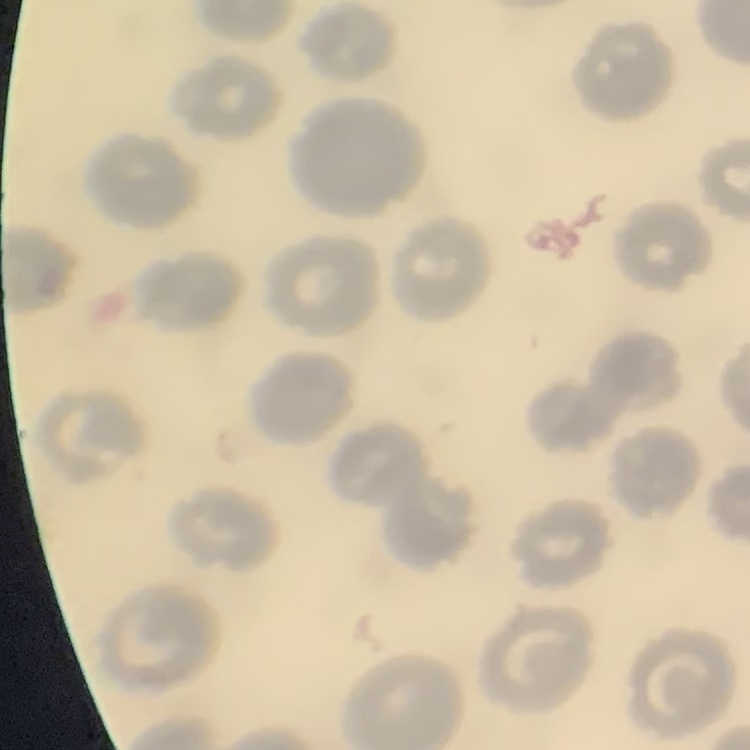
Summary:
  - Red blood cell morphology: no rouleaux formation
  - Preparation: thin blood smear
  - Image type: square crop of a larger photomicrograph
  - Stain: Field's or Giemsa